Locate and identify every blood parasite.
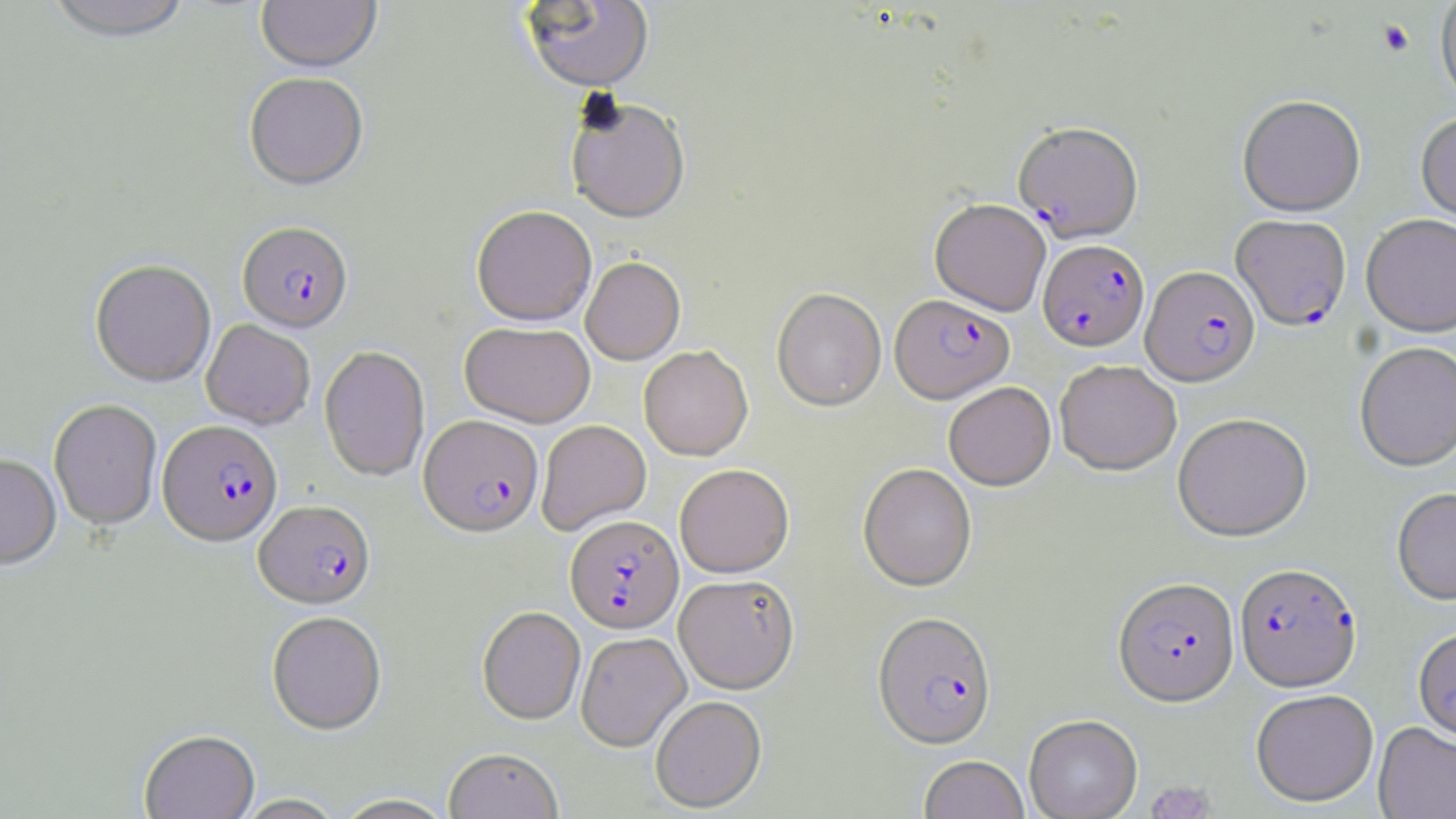

Approximate bounding boxes as (x1,y1)-(x2,y2) corner pairs in pixels.
Plasmodium falciparum-infected red blood cells: (1014,125)-(1143,244), (1230,216)-(1351,333), (237,222)-(354,335), (1037,240)-(1149,353), (1140,267)-(1260,389), (890,296)-(1015,406), (418,416)-(544,538), (158,421)-(283,549), (255,501)-(375,611), (566,516)-(684,634), (1234,564)-(1363,695), (1112,579)-(1240,711), (872,613)-(998,752), (1412,629)-(1456,748).
No Plasmodium ovale, Plasmodium malariae, Plasmodium vivax, Babesia divergens, or Trypanosoma brucei observed.

slide-level diagnosis = Plasmodium falciparum
image size = 1456×819 pixels
magnification = 1000x
stain = May-Grünwald-Giemsa
preparation = thin blood film
uninfected red blood cell locations = approximate bounding boxes as (x1,y1)-(x2,y2) corner pairs in pixels: (42,0)-(195,43), (521,0)-(654,95), (256,1)-(381,74), (1436,1)-(1456,112), (244,73)-(368,192), (1237,97)-(1366,219), (565,101)-(691,226), (1415,115)-(1456,232), (929,201)-(1051,316), (471,208)-(596,328), (1361,215)-(1456,339), (581,258)-(685,366), (90,260)-(216,388), (772,289)-(887,413), (201,320)-(315,430), (460,323)-(595,429), (1354,343)-(1456,474), (639,346)-(753,460), (319,347)-(430,482), (1055,361)-(1181,477), (943,382)-(1056,491), (49,400)-(162,532), (1173,414)-(1313,544), (537,420)-(651,535), (0,455)-(61,573), (858,464)-(978,594), (674,465)-(794,579), (1392,488)-(1456,607), (674,575)-(800,695), (477,607)-(586,726), (267,612)-(387,736), (576,634)-(691,752), (1250,692)-(1379,809), (650,697)-(767,813), (1024,717)-(1142,819), (1373,724)-(1456,819), (139,731)-(260,818), (444,748)-(563,819), (918,757)-(1030,819), (332,794)-(457,819), (233,795)-(347,819)
modality = light microscopy
platelet locations = approximate bounding boxes as (x1,y1)-(x2,y2) corner pairs in pixels: (1377,20)-(1415,57), (1146,781)-(1217,819)
field of view = single